State which parasite is depicted.
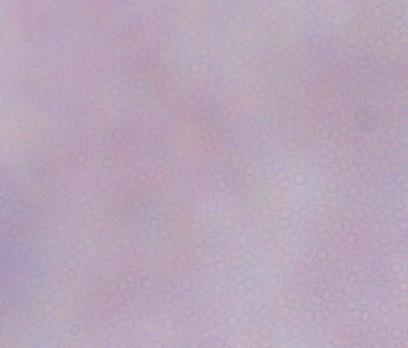
This is a trypanosome.

Summary:
  - Magnification: 1000x
  - Modality: photomicrograph